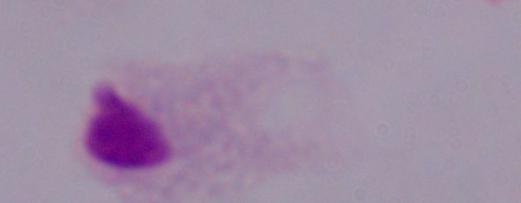
magnification = 1000x
modality = micrograph
identification = trichomonad